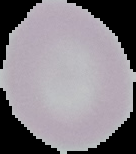 Result: no malaria parasites seen. Cell region segmented out of the field of view; the surrounding area is masked to black. From a thin blood film. Image is 136×154 pixels.